Locate every Plasmodium falciparum parasite and give its life-cycle stage, and locate every leukocyte and any debris.
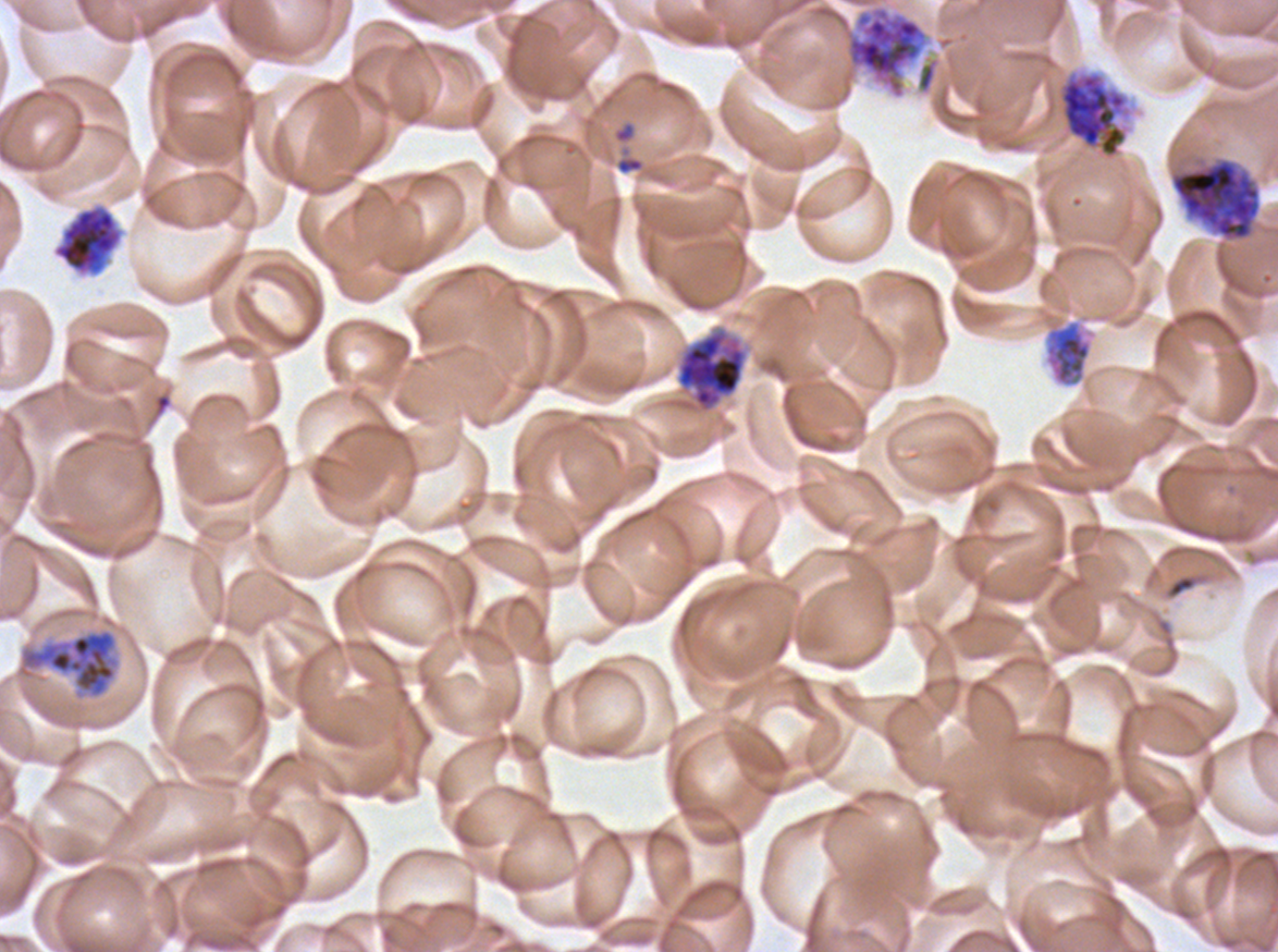
Approximate bounding boxes as (x1, y1, x2, y2) in pixels.
Early schizonts: (1170, 156, 1261, 242), (1043, 319, 1093, 388), (675, 328, 748, 413), (16, 628, 121, 701).
Late schizonts: (844, 6, 928, 99), (1059, 71, 1128, 159).
Segmenters: (53, 205, 123, 275).
Debris: (1166, 574, 1197, 599).
No rings, late-ring/early-trophozoite forms, mid trophozoites, late trophozoites, gametocytes, or leukocytes observed.

Summary:
  - Preparation: thin blood smear
  - Life-cycle stages observed: early schizont, late schizont, segmenter
  - Specimen: ex-vivo Plasmodium falciparum culture from a patient in The Gambia, grown for 24 to 48 hours
  - Image size: 1278×952 pixels
  - Stain: Giemsa
  - Field of view: one sub-image of a larger composite